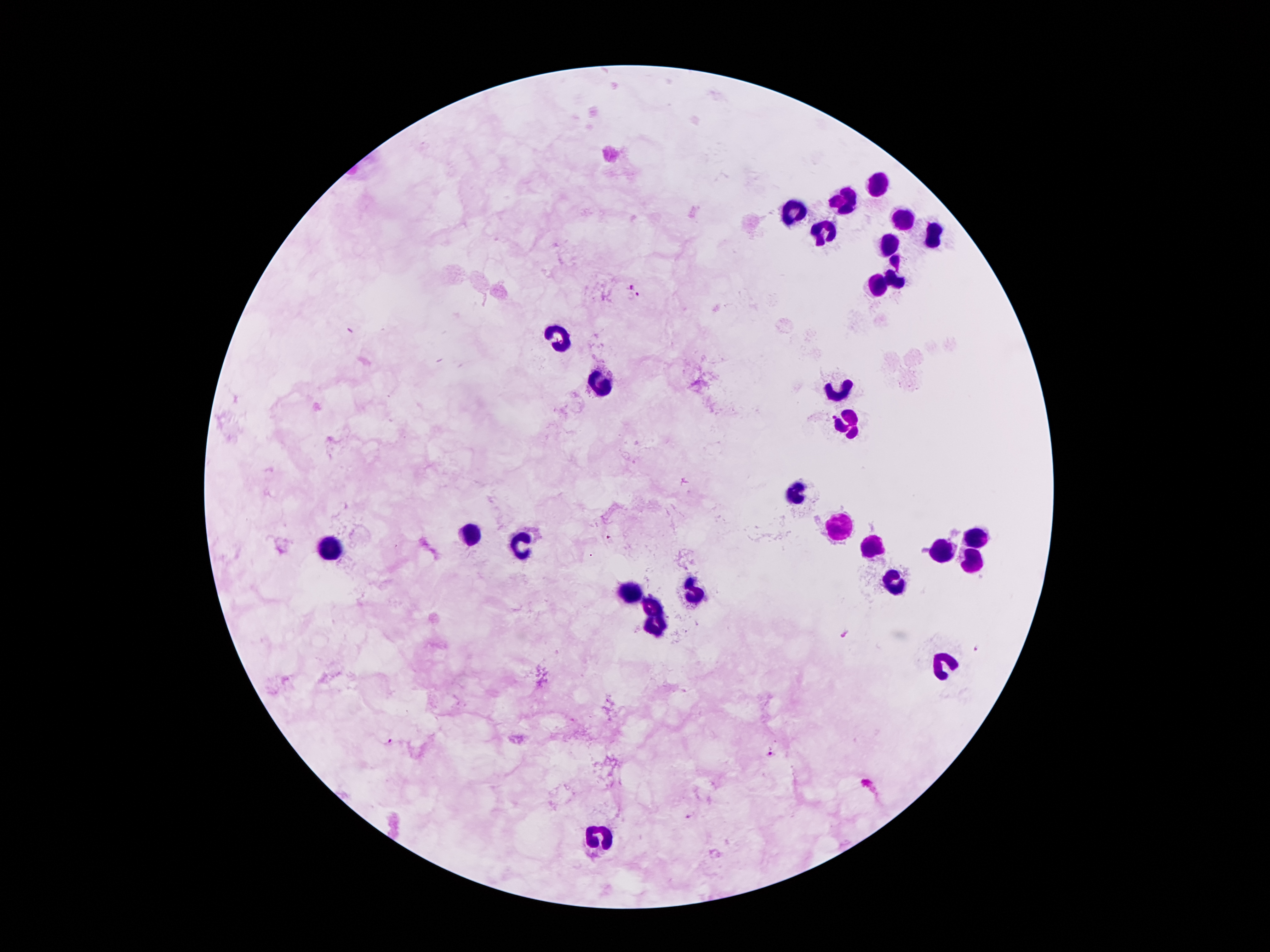

field_of_view: one from this slide
leukocyte_locations: 'approximate object centers, in pixels from the top-left corner: (x=878, y=186), (x=847, y=197), (x=790, y=211), (x=900, y=219), (x=823, y=230), (x=934, y=239), (x=887, y=244), (x=894, y=271), (x=878, y=286), (x=560, y=339), (x=600, y=381), (x=836, y=386), (x=847, y=415), (x=792, y=492), (x=841, y=529), (x=976, y=535), (x=476, y=536), (x=525, y=542), (x=872, y=542), (x=335, y=543), (x=940, y=545), (x=973, y=560), (x=894, y=580), (x=693, y=586), (x=629, y=591), (x=651, y=604), (x=653, y=626), (x=595, y=838)'
preparation: thick blood film
malaria_parasite_locations: 'approximate object centers, in pixels from the top-left corner: (x=631, y=285), (x=639, y=293), (x=609, y=540), (x=848, y=634), (x=977, y=649), (x=388, y=742), (x=772, y=755), (x=866, y=782), (x=689, y=816)'
patient_malaria_status: infected with Plasmodium falciparum
stain: Giemsa
capture: smartphone through the microscope eyepiece
magnification: 100x
image_size: 1270×952 pixels